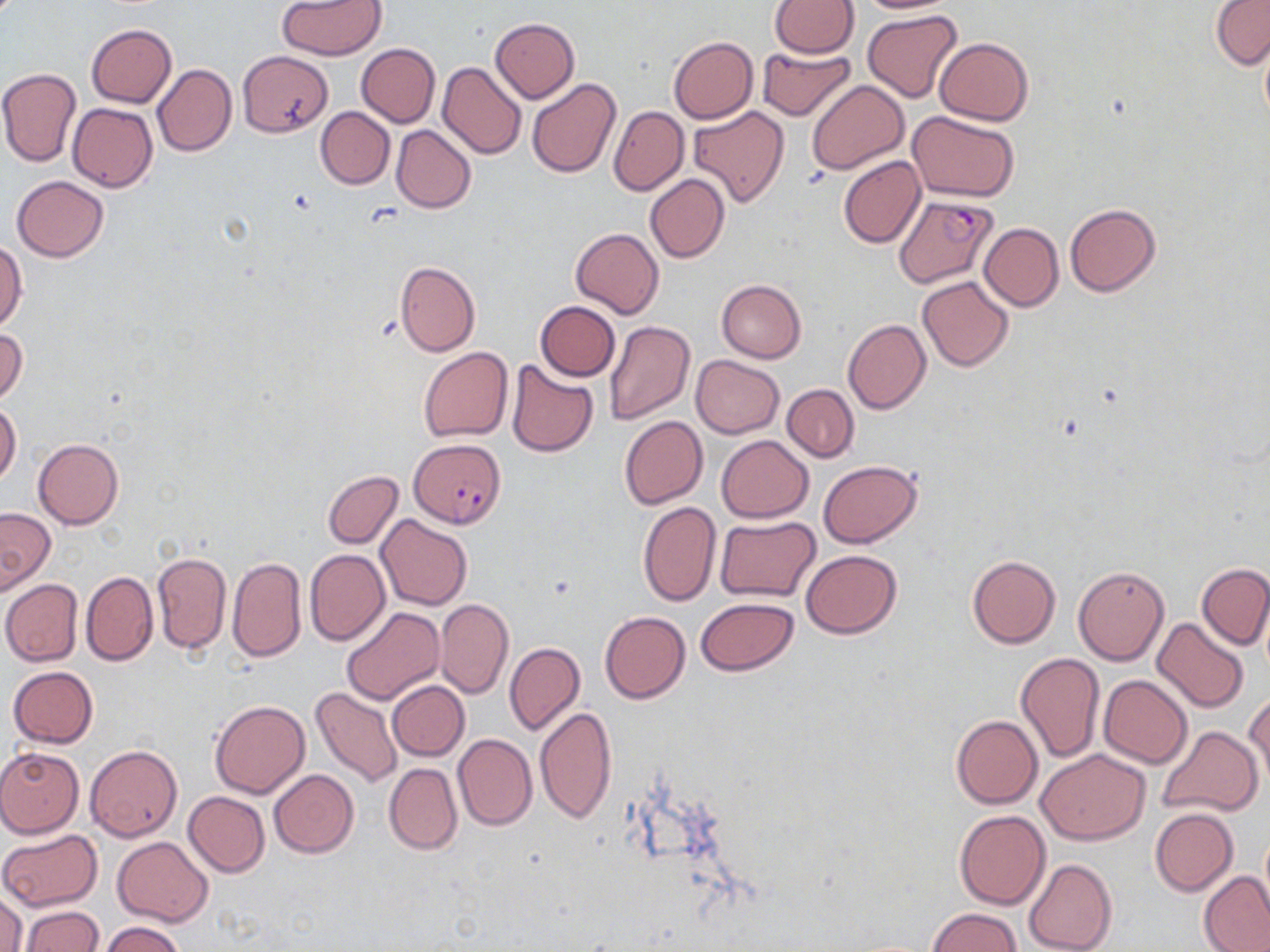
Summary:
  - Coordinate format: approximate bounding boxes as (x1, y1, x2, y2) in pixels
  - Uninfected red blood cell locations: (770, 0, 860, 57), (851, 0, 960, 14), (1211, 0, 1270, 71), (277, 1, 386, 60), (862, 9, 963, 103), (489, 18, 580, 102), (87, 23, 176, 108), (1259, 29, 1270, 129), (668, 36, 758, 123), (934, 37, 1032, 126), (356, 44, 440, 127), (757, 46, 855, 121), (237, 50, 334, 136), (437, 61, 525, 159), (152, 63, 236, 156), (0, 67, 80, 168), (526, 77, 621, 177), (806, 80, 909, 174), (68, 102, 157, 191), (608, 106, 687, 196), (687, 106, 790, 206), (315, 107, 395, 189), (907, 110, 1018, 200), (390, 125, 476, 213), (838, 155, 926, 248), (645, 174, 729, 263), (11, 175, 108, 262), (1065, 204, 1161, 296), (979, 222, 1063, 310), (570, 227, 663, 319), (0, 240, 26, 332), (394, 261, 480, 356), (916, 275, 1014, 372), (716, 279, 806, 363), (534, 301, 620, 381), (843, 319, 930, 415), (604, 321, 694, 424), (0, 327, 27, 406), (418, 347, 513, 442), (690, 356, 783, 438), (506, 360, 598, 457), (782, 384, 859, 462), (0, 401, 21, 486), (620, 416, 707, 509), (716, 435, 813, 523), (33, 439, 123, 529), (817, 460, 922, 548), (323, 470, 403, 548), (637, 501, 720, 606), (0, 507, 55, 594), (376, 515, 472, 611), (716, 517, 822, 603), (305, 550, 389, 646), (801, 550, 902, 639), (152, 552, 231, 654), (966, 555, 1060, 647), (226, 556, 306, 664), (1198, 565, 1270, 650), (1072, 566, 1169, 665), (81, 571, 158, 665), (1, 579, 83, 666), (695, 597, 798, 675), (436, 599, 513, 699), (339, 608, 444, 705), (600, 611, 690, 704), (1151, 617, 1249, 712), (505, 642, 585, 736), (1015, 652, 1104, 764), (7, 666, 99, 748), (1099, 675, 1193, 768), (387, 681, 468, 761), (311, 687, 403, 788), (1246, 692, 1269, 789), (210, 700, 309, 798), (535, 707, 617, 825), (951, 715, 1042, 808), (1157, 725, 1264, 818), (453, 733, 537, 831), (85, 745, 182, 840), (0, 748, 84, 837), (1038, 749, 1149, 844), (383, 762, 462, 855), (268, 769, 359, 858), (183, 791, 270, 877), (1150, 809, 1238, 896), (954, 810, 1050, 909), (0, 828, 103, 911), (1258, 828, 1270, 915), (112, 837, 213, 926), (1024, 858, 1117, 952), (1198, 871, 1270, 952), (0, 889, 26, 952), (20, 906, 104, 952), (928, 908, 1020, 952), (101, 921, 183, 952)
  - Plasmodium falciparum-infected red blood cell locations: (894, 193, 997, 289), (411, 438, 506, 528)
  - Slide-level diagnosis: Plasmodium falciparum
  - Stain: May-Grünwald-Giemsa
  - Image size: 1270×952 pixels
  - Magnification: 1000x
  - Modality: optical microscopy
  - Field of view: single
  - Preparation: thin blood film